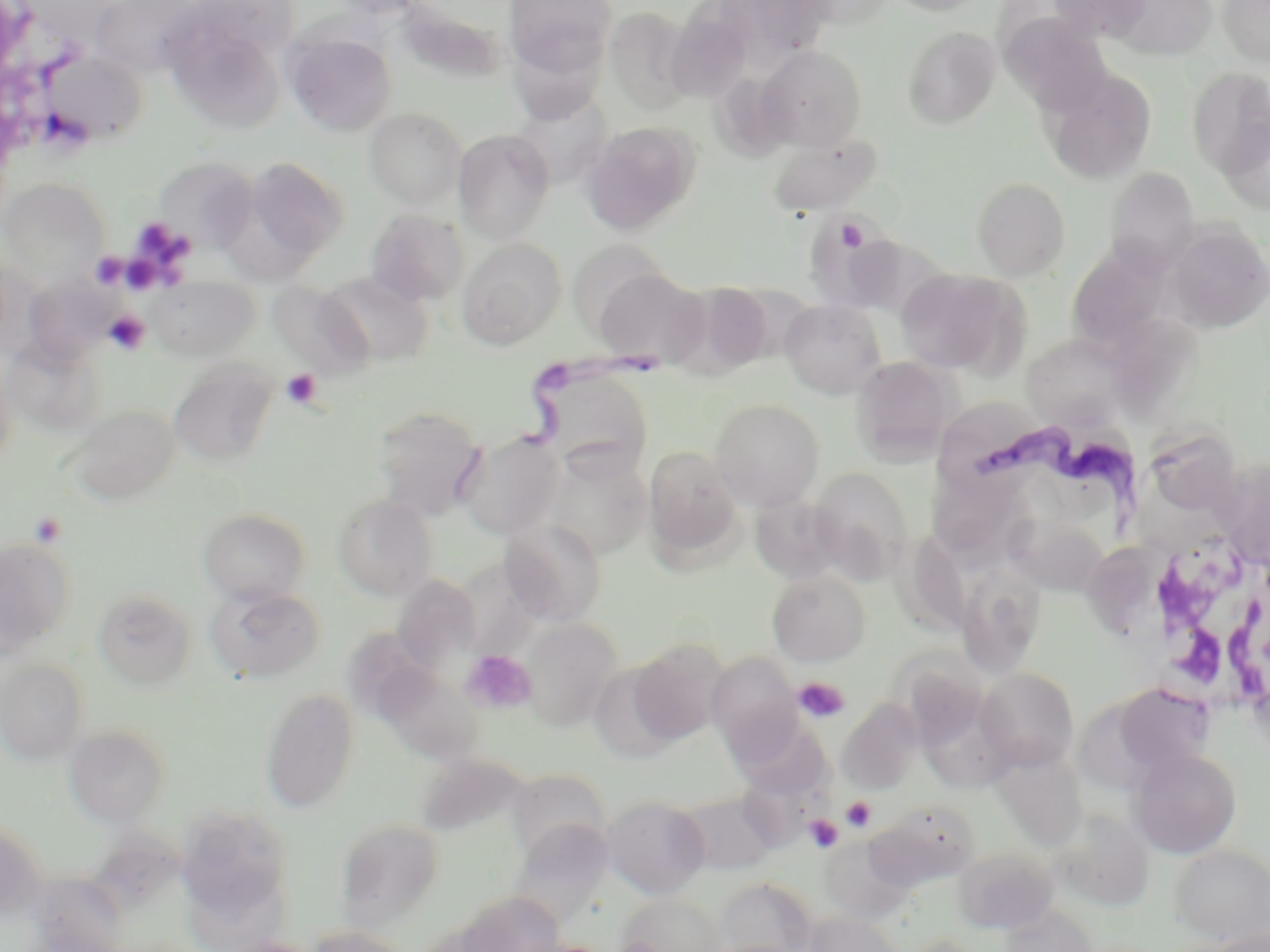

Summary:
  - Coordinate format: approximate bounding boxes as named x1/y1/x2/y2 corners in pixels
  - Uninfected red blood cell locations: (x1=91, y1=0, x2=201, y2=78), (x1=503, y1=0, x2=616, y2=79), (x1=886, y1=0, x2=990, y2=16), (x1=1048, y1=0, x2=1152, y2=42), (x1=1218, y1=0, x2=1270, y2=66), (x1=708, y1=1, x2=836, y2=66), (x1=1110, y1=1, x2=1219, y2=60), (x1=392, y1=2, x2=509, y2=84), (x1=602, y1=6, x2=696, y2=116), (x1=999, y1=12, x2=1115, y2=116), (x1=671, y1=22, x2=758, y2=103), (x1=169, y1=25, x2=280, y2=137), (x1=902, y1=26, x2=1001, y2=129), (x1=287, y1=30, x2=397, y2=137), (x1=756, y1=44, x2=867, y2=150), (x1=43, y1=52, x2=149, y2=145), (x1=1041, y1=67, x2=1157, y2=185), (x1=1186, y1=67, x2=1270, y2=179), (x1=713, y1=78, x2=810, y2=166), (x1=506, y1=101, x2=616, y2=191), (x1=364, y1=107, x2=467, y2=209), (x1=1217, y1=117, x2=1270, y2=216), (x1=580, y1=121, x2=701, y2=234), (x1=453, y1=129, x2=555, y2=243), (x1=768, y1=132, x2=882, y2=216), (x1=154, y1=155, x2=259, y2=253), (x1=246, y1=157, x2=349, y2=259), (x1=1102, y1=168, x2=1200, y2=274), (x1=1, y1=178, x2=109, y2=285), (x1=972, y1=180, x2=1070, y2=282), (x1=364, y1=209, x2=469, y2=306), (x1=804, y1=214, x2=897, y2=306), (x1=1166, y1=224, x2=1269, y2=332), (x1=456, y1=237, x2=566, y2=350), (x1=855, y1=239, x2=955, y2=334), (x1=567, y1=240, x2=675, y2=339), (x1=1066, y1=244, x2=1172, y2=347), (x1=594, y1=267, x2=710, y2=368), (x1=896, y1=268, x2=1022, y2=374), (x1=321, y1=271, x2=435, y2=367), (x1=144, y1=274, x2=260, y2=362), (x1=267, y1=280, x2=374, y2=379), (x1=677, y1=280, x2=777, y2=376), (x1=32, y1=283, x2=138, y2=359), (x1=780, y1=299, x2=886, y2=399), (x1=1112, y1=318, x2=1205, y2=420), (x1=1021, y1=333, x2=1128, y2=429), (x1=2, y1=335, x2=104, y2=438), (x1=0, y1=354, x2=17, y2=470), (x1=851, y1=356, x2=960, y2=464), (x1=169, y1=359, x2=278, y2=469), (x1=535, y1=363, x2=655, y2=476), (x1=709, y1=399, x2=825, y2=510), (x1=69, y1=404, x2=181, y2=504), (x1=372, y1=406, x2=487, y2=520), (x1=1151, y1=416, x2=1239, y2=518), (x1=455, y1=432, x2=565, y2=539), (x1=642, y1=445, x2=744, y2=564), (x1=541, y1=451, x2=652, y2=562), (x1=810, y1=467, x2=914, y2=581), (x1=1228, y1=468, x2=1270, y2=560), (x1=924, y1=469, x2=1034, y2=565), (x1=333, y1=494, x2=438, y2=601), (x1=751, y1=494, x2=848, y2=585), (x1=198, y1=508, x2=311, y2=605), (x1=1004, y1=516, x2=1110, y2=596), (x1=501, y1=520, x2=608, y2=627), (x1=890, y1=531, x2=972, y2=637), (x1=0, y1=538, x2=74, y2=654), (x1=1088, y1=541, x2=1161, y2=642), (x1=956, y1=565, x2=1046, y2=677), (x1=767, y1=569, x2=871, y2=666), (x1=391, y1=574, x2=483, y2=673), (x1=205, y1=583, x2=326, y2=684), (x1=93, y1=588, x2=197, y2=689), (x1=518, y1=617, x2=623, y2=730), (x1=349, y1=629, x2=453, y2=728), (x1=628, y1=639, x2=729, y2=744), (x1=706, y1=652, x2=803, y2=756), (x1=891, y1=653, x2=989, y2=748), (x1=0, y1=659, x2=90, y2=763), (x1=586, y1=661, x2=685, y2=762), (x1=976, y1=668, x2=1079, y2=770), (x1=378, y1=672, x2=486, y2=757), (x1=1120, y1=682, x2=1214, y2=756), (x1=260, y1=687, x2=360, y2=813), (x1=836, y1=698, x2=922, y2=796), (x1=1079, y1=701, x2=1153, y2=793), (x1=727, y1=711, x2=835, y2=802), (x1=64, y1=723, x2=172, y2=826), (x1=990, y1=748, x2=1088, y2=852), (x1=1129, y1=748, x2=1242, y2=858), (x1=422, y1=755, x2=521, y2=841), (x1=511, y1=768, x2=607, y2=851), (x1=674, y1=789, x2=782, y2=875), (x1=603, y1=794, x2=709, y2=898), (x1=866, y1=800, x2=980, y2=888), (x1=1051, y1=810, x2=1154, y2=911), (x1=171, y1=814, x2=288, y2=917), (x1=513, y1=817, x2=617, y2=928), (x1=337, y1=818, x2=445, y2=929), (x1=0, y1=821, x2=47, y2=917), (x1=820, y1=838, x2=913, y2=923), (x1=1170, y1=844, x2=1270, y2=946), (x1=954, y1=846, x2=1058, y2=933), (x1=36, y1=870, x2=123, y2=952), (x1=716, y1=877, x2=817, y2=952), (x1=453, y1=891, x2=567, y2=952), (x1=617, y1=893, x2=728, y2=952), (x1=999, y1=905, x2=1098, y2=952), (x1=803, y1=911, x2=903, y2=952), (x1=307, y1=924, x2=414, y2=952), (x1=1202, y1=926, x2=1270, y2=952), (x1=897, y1=934, x2=987, y2=952), (x1=221, y1=937, x2=326, y2=952)
  - Trypanosoma brucei locations: (x1=485, y1=348, x2=669, y2=459), (x1=973, y1=415, x2=1144, y2=542)
  - Platelet locations: (x1=836, y1=218, x2=869, y2=252), (x1=105, y1=311, x2=149, y2=354), (x1=281, y1=369, x2=323, y2=409), (x1=30, y1=511, x2=67, y2=549), (x1=463, y1=650, x2=536, y2=713), (x1=793, y1=677, x2=850, y2=723), (x1=841, y1=796, x2=876, y2=832), (x1=803, y1=814, x2=844, y2=853)
  - White blood cell locations: (x1=1143, y1=537, x2=1268, y2=711)
  - Slide-level diagnosis: Trypanosoma brucei
  - Image size: 1270×952 pixels
  - Stain: May-Grünwald-Giemsa
  - Field of view: single
  - Preparation: thin blood smear
  - Modality: optical microscopy
  - Magnification: 1000x